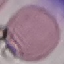
Result: no malaria parasites detected. Photographed with a smartphone camera at the microscope eyepiece. Thin blood film. Giemsa-stained preparation. Automatically extracted cell patch, resized to 64 × 64 pixels.